Point out each leukocyte.
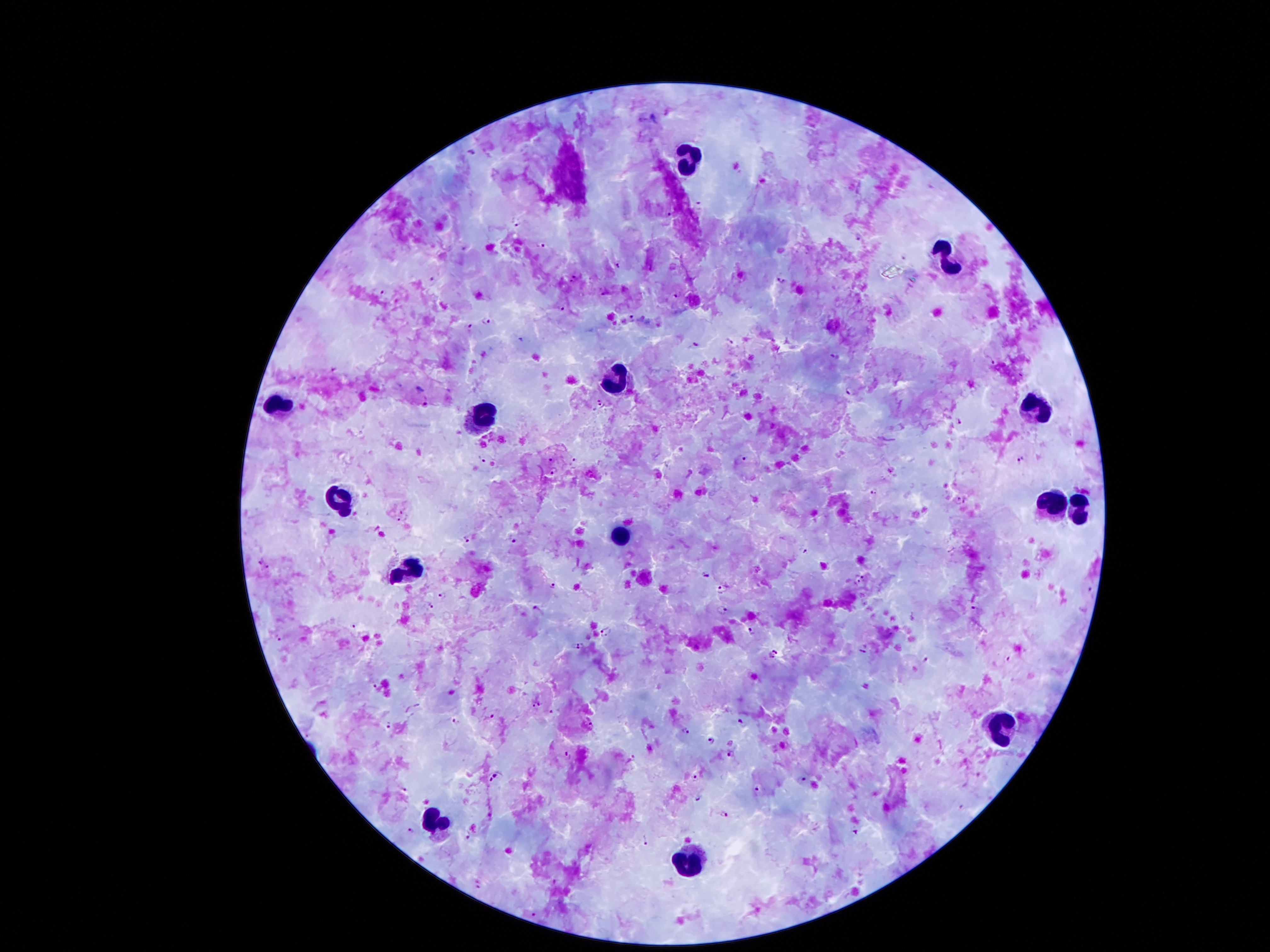

Approximate centers as {x, y} in pixels.
Leukocytes: {693, 159}, {949, 257}, {615, 381}, {277, 402}, {1037, 409}, {483, 417}, {336, 499}, {1054, 499}, {1082, 514}, {620, 537}, {405, 568}, {1006, 726}, {435, 816}, {691, 862}.

Malaria parasite locations: {472, 153}, {518, 223}, {859, 238}, {539, 246}, {578, 274}, {782, 279}, {432, 282}, {383, 293}, {681, 294}, {563, 307}, {631, 317}, {486, 320}, {469, 326}, {730, 341}, {695, 346}, {836, 354}, {992, 361}, {850, 391}, {426, 400}, {960, 422}, {573, 458}, {744, 458}, {1022, 458}, {481, 459}, {551, 461}, {553, 470}, {872, 493}, {961, 499}, {403, 517}, {467, 538}, {511, 540}, {264, 563}, {707, 573}, {862, 579}, {553, 586}, {723, 590}, {1093, 593}, {442, 594}, {431, 604}, {973, 606}, {723, 609}, {536, 610}, {353, 626}, {752, 631}, {604, 633}, {279, 636}, {577, 648}, {773, 653}, {925, 659}, {1009, 661}, {376, 685}, {536, 704}, {556, 710}, {489, 715}, {457, 720}, {591, 722}, {390, 724}, {742, 724}, {687, 731}, {708, 740}, {729, 753}, {568, 756}, {630, 758}, {497, 778}, {693, 779}, {803, 779}, {405, 790}, {759, 791}, {698, 798}, {724, 811}, {411, 830}, {850, 832}, {644, 837}, {467, 838}, {553, 882}, {478, 885}, {534, 914}. 100x magnification. Smartphone photograph taken through the microscope eyepiece. Image is 1270×952 pixels. One field from this slide. Giemsa-stained preparation. Patient malaria status: positive for Plasmodium falciparum. Thick blood smear.